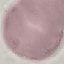

result = no malaria parasites seen
preparation = thin blood smear
stain = Giemsa
image type = cell patch, automatically extracted from a larger field of view and resized to 64 × 64 pixels
capture = smartphone through the microscope eyepiece